Identify the parasite.
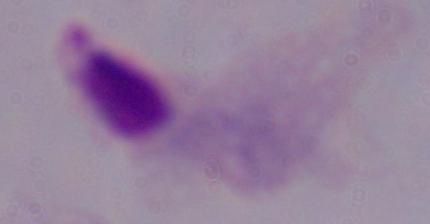
A trichomonad.

Summary:
  - Modality: micrograph
  - Magnification: 1000x